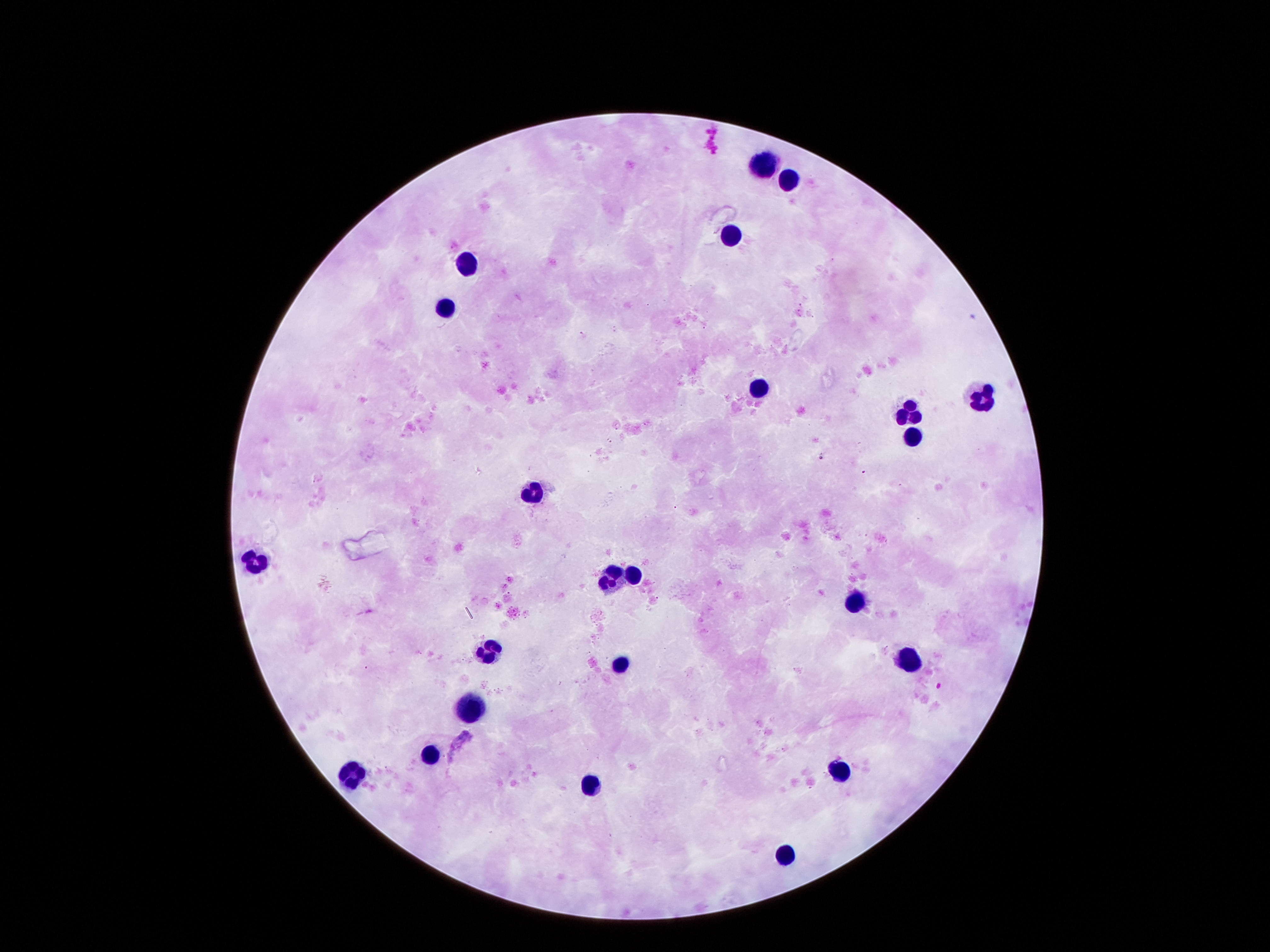

capture: smartphone camera through the microscope eyepiece
stain: Giemsa
image_size: 1270×952 pixels
patient_malaria_status: negative
magnification: 100x
field_of_view: one from this slide
preparation: thick peripheral-blood smear
leukocyte_locations: 'approximate centers as {x, y} in pixels: {764, 163}, {788, 179}, {731, 236}, {469, 259}, {445, 305}, {758, 386}, {986, 389}, {911, 410}, {911, 434}, {535, 488}, {256, 557}, {614, 572}, {635, 572}, {857, 598}, {484, 647}, {908, 658}, {620, 662}, {463, 706}, {430, 749}, {842, 766}, {349, 773}, {587, 782}, {785, 854}'